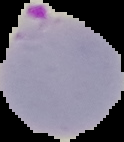
Summary:
  - Preparation: thin blood film
  - Result: malaria parasites identified
  - Image size: 124×142 pixels
  - Image type: segmented cell region with the area outside set to black